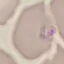
Summary:
  - Malaria status: parasitized
  - Stain: Giemsa
  - Preparation: thin smear
  - Image type: automatically extracted cell patch, resized to 64 × 64 pixels
  - Capture: smartphone camera at the microscope eyepiece